Report the malaria status of this cell.
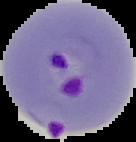
Parasitized.

From a thin blood film. Segmented cell region on a black background. Image is 136×142 pixels.